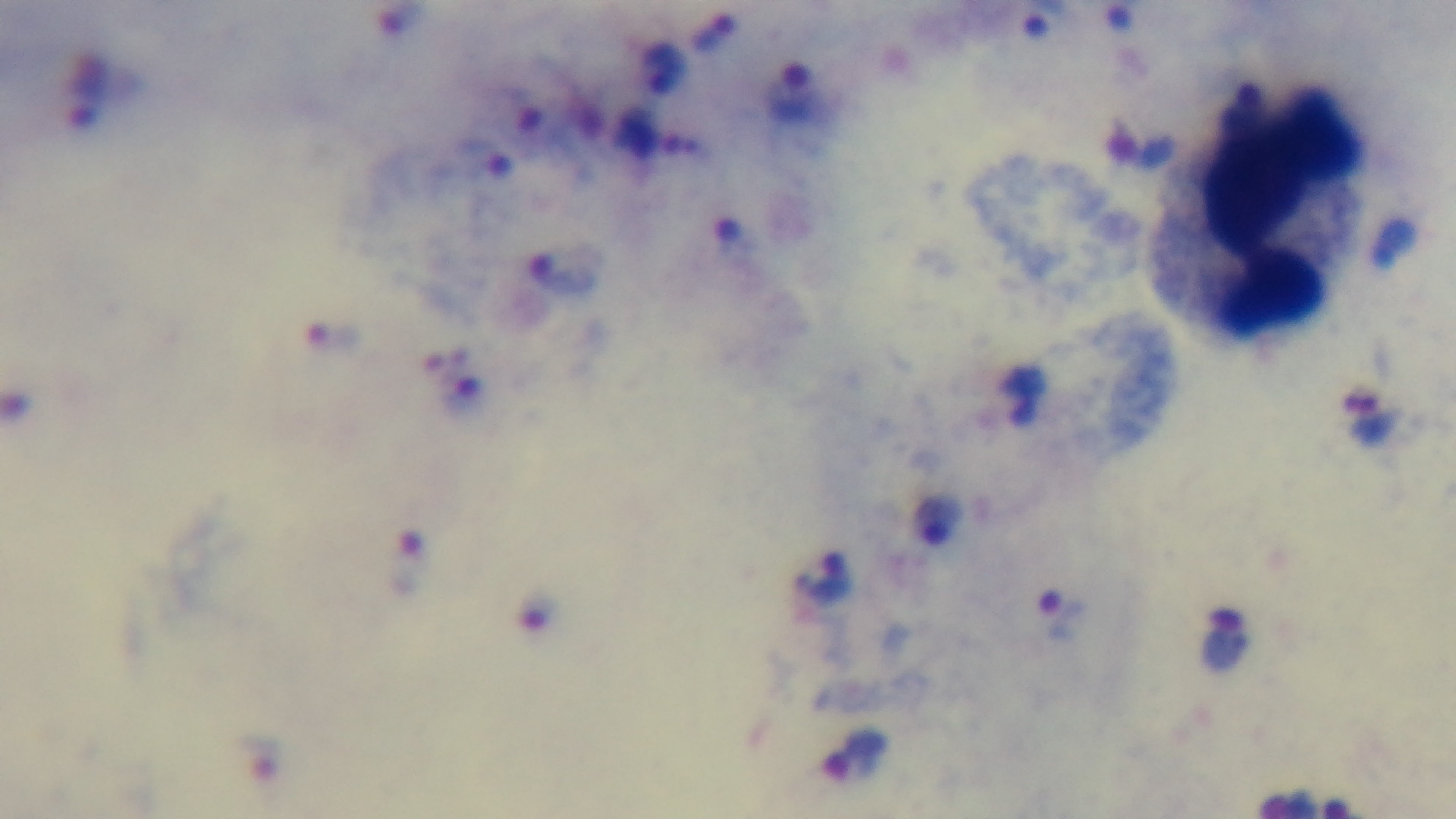
Summary:
  - Malaria status: positive
  - Stain: Giemsa
  - Modality: light microscopy
  - Objective: 100x oil immersion
  - Capture: mounted 4K digital camera
  - Field of view: single
  - Preparation: thick